Comment on the morphology of the red blood cells.
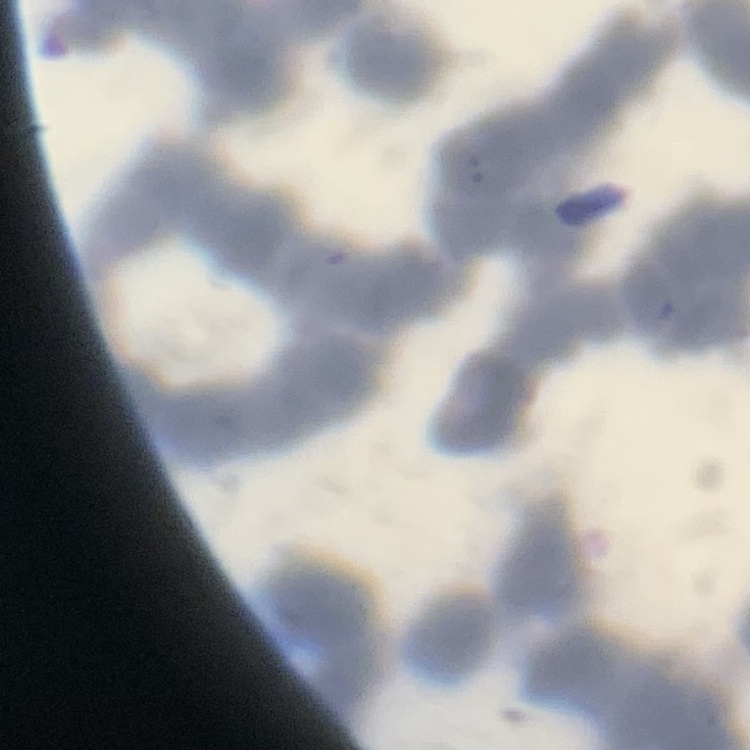

Rouleaux formation.

preparation = thin peripheral smear
stain = Field's or Giemsa
image type = one tile cut from a larger photomicrograph